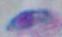

{
  "magnification": "1000x",
  "modality": "photomicrograph",
  "identification": "Toxoplasma gondii"
}